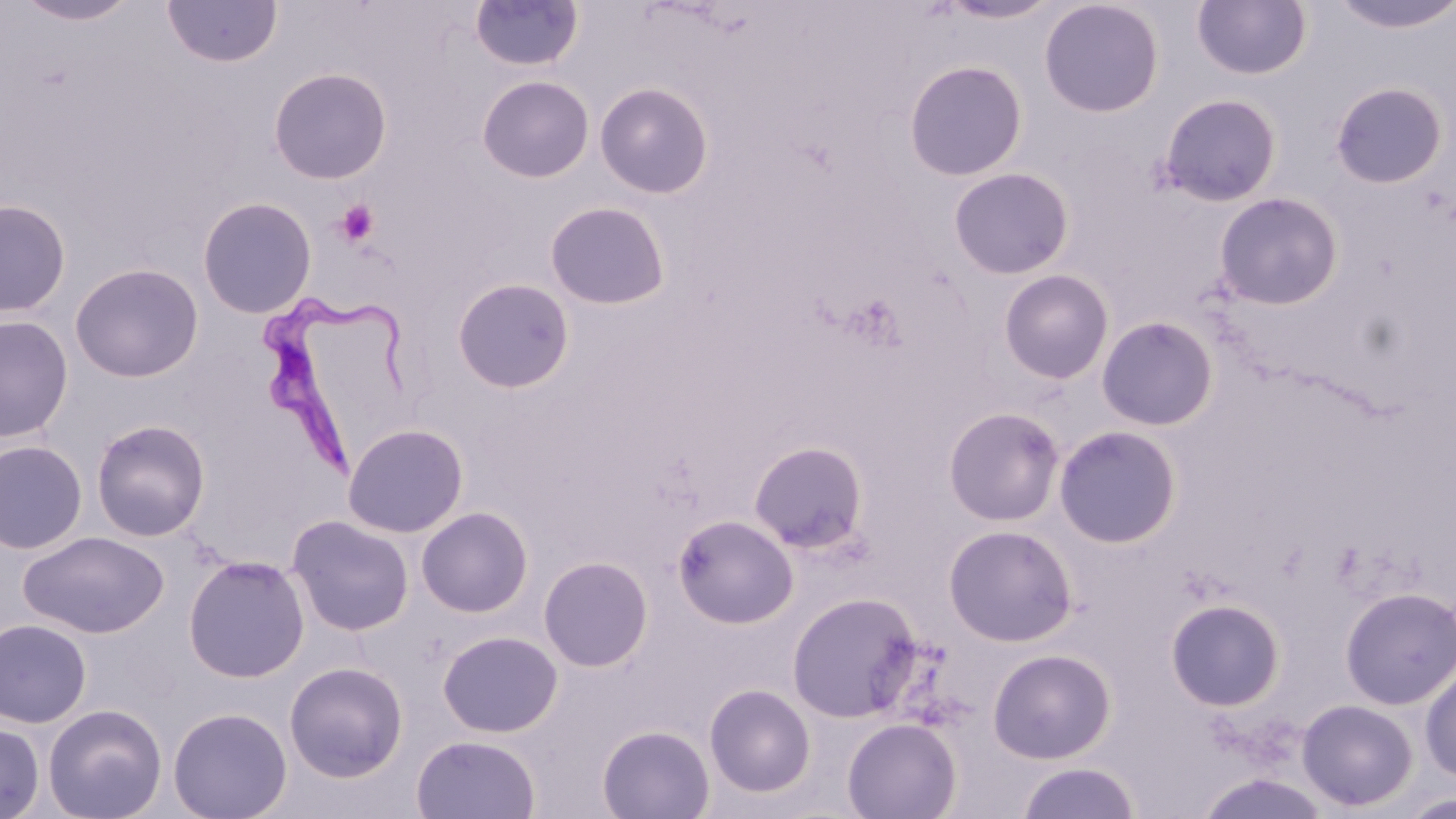
slide-level diagnosis = Trypanosoma brucei
preparation = thin blood smear
magnification = 1000x
image size = 1456×819 pixels
modality = optical microscopy
platelet locations = approximate bounding boxes as (x1,y1)-(x2,y2) corner pairs in pixels: (334,199)-(380,247)
stain = May-Grünwald-Giemsa
field of view = one of a larger specimen
Trypanosoma brucei locations = approximate bounding boxes as (x1,y1)-(x2,y2) corner pairs in pixels: (263,290)-(420,485)
uninfected red blood cell locations = approximate bounding boxes as (x1,y1)-(x2,y2) corner pairs in pixels: (162,0)-(283,68), (936,0)-(1063,25), (1039,0)-(1164,118), (1192,0)-(1311,80), (1326,0)-(1456,34), (14,1)-(140,26), (469,1)-(584,72), (903,59)-(1028,181), (268,67)-(392,184), (476,75)-(595,183), (595,81)-(714,199), (1330,81)-(1449,188), (1157,92)-(1283,207), (948,167)-(1074,280), (1213,192)-(1344,309), (197,196)-(317,318), (0,198)-(71,317), (544,201)-(670,309), (69,262)-(204,382), (998,269)-(1114,384), (451,278)-(575,393), (0,314)-(74,442), (1097,316)-(1219,431), (943,407)-(1066,525), (90,419)-(211,542), (342,423)-(469,538), (1053,425)-(1183,548), (0,440)-(88,554), (749,441)-(869,554), (416,507)-(534,617), (672,514)-(799,629), (287,515)-(414,636), (943,523)-(1078,646), (18,531)-(169,638), (183,555)-(310,683), (538,555)-(654,672), (1340,587)-(1456,710), (786,591)-(923,723), (1166,598)-(1285,712), (0,619)-(92,728), (437,630)-(563,737), (987,648)-(1116,764), (284,661)-(408,782), (1420,663)-(1456,784), (704,684)-(816,798), (1297,698)-(1419,811), (43,704)-(167,819), (168,706)-(293,819), (842,717)-(962,819), (0,721)-(45,818), (597,724)-(715,818), (411,734)-(541,818), (1016,761)-(1142,819), (1194,771)-(1332,818), (1396,792)-(1455,818)